State which cell type is depicted.
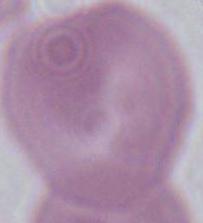
This is an erythrocyte.

Summary:
  - Modality: photomicrograph
  - Magnification: 1000x